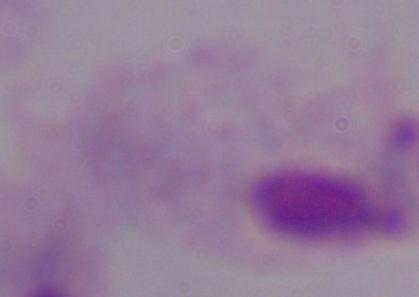
A trichomonad is seen. Micrograph. Captured at 1000x magnification.